Classify this cell by malaria status.
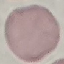

It is uninfected.

Cell patch, automatically extracted from a larger field of view and resized to 64 × 64 pixels. Giemsa stain. Thin blood film. Acquired by smartphone through the microscope eyepiece.